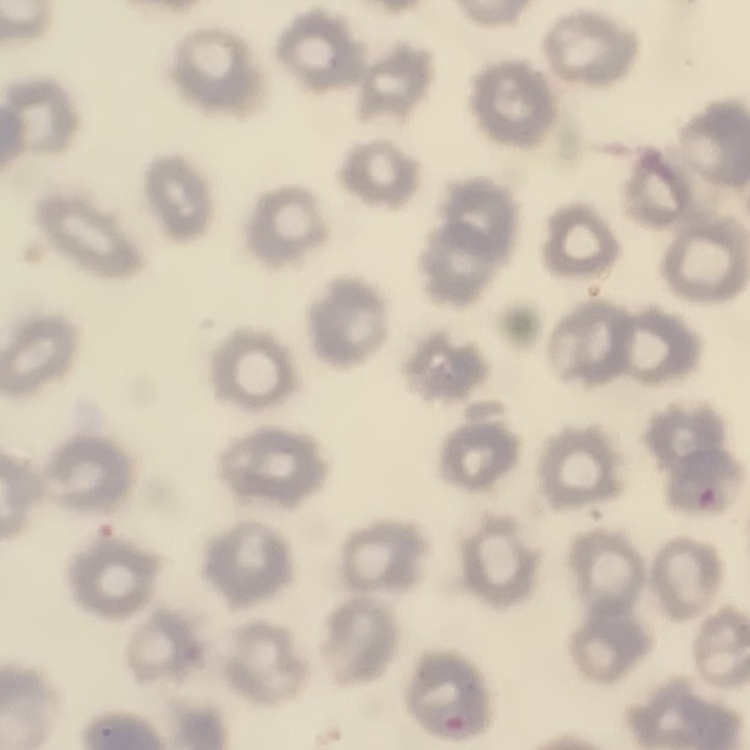
Summary:
  - Erythrocyte morphology: no rouleaux formation
  - Image type: one tile cut from a larger photomicrograph
  - Stain: Field's or Giemsa
  - Preparation: thin peripheral smear